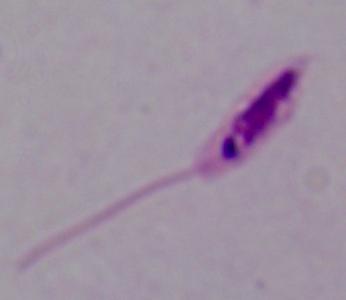

identification = Leishmania
magnification = 1000x
modality = photomicrograph